Assess this cell for malaria.
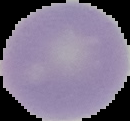

It is uninfected.

Image is 130×121 pixels. Segmented cell region on a black background. From a thin blood film.